Report the malaria status of this cell.
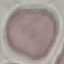

Uninfected.

{
  "image_type": "cell patch, automatically extracted from a larger field of view and resized to 64 × 64 pixels",
  "capture": "smartphone camera at the microscope eyepiece",
  "preparation": "thin blood film",
  "stain": "Giemsa"
}